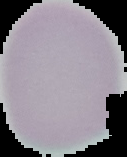

preparation = thin blood film
image type = segmented cell region on a black background
malaria status = uninfected
image size = 127×157 pixels